Identify the parasite.
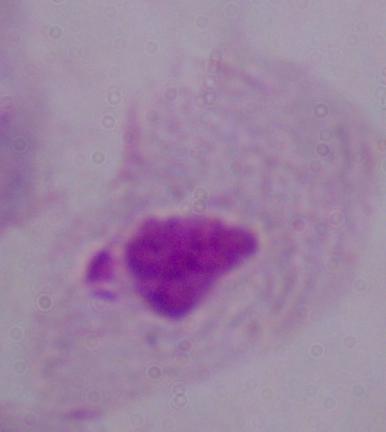

A trichomonad.

Photomicrograph. 1000x magnification.